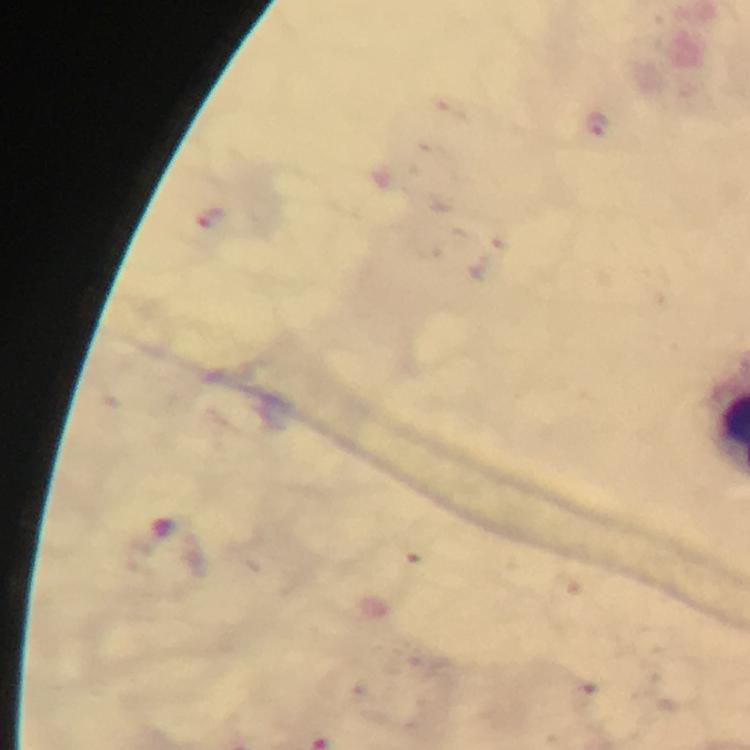
preparation = thick smear
stain = Giemsa
malaria parasite locations = approximate object centers, in pixels from the top-left corner: (x=596, y=122), (x=585, y=698)
image size = 750×750 pixels
cropped from = one field of view
capture = smartphone photograph through a microscope
magnification = 100x
immersion oil = applied
context = from a malaria diagnostic workup